Evaluate for malaria.
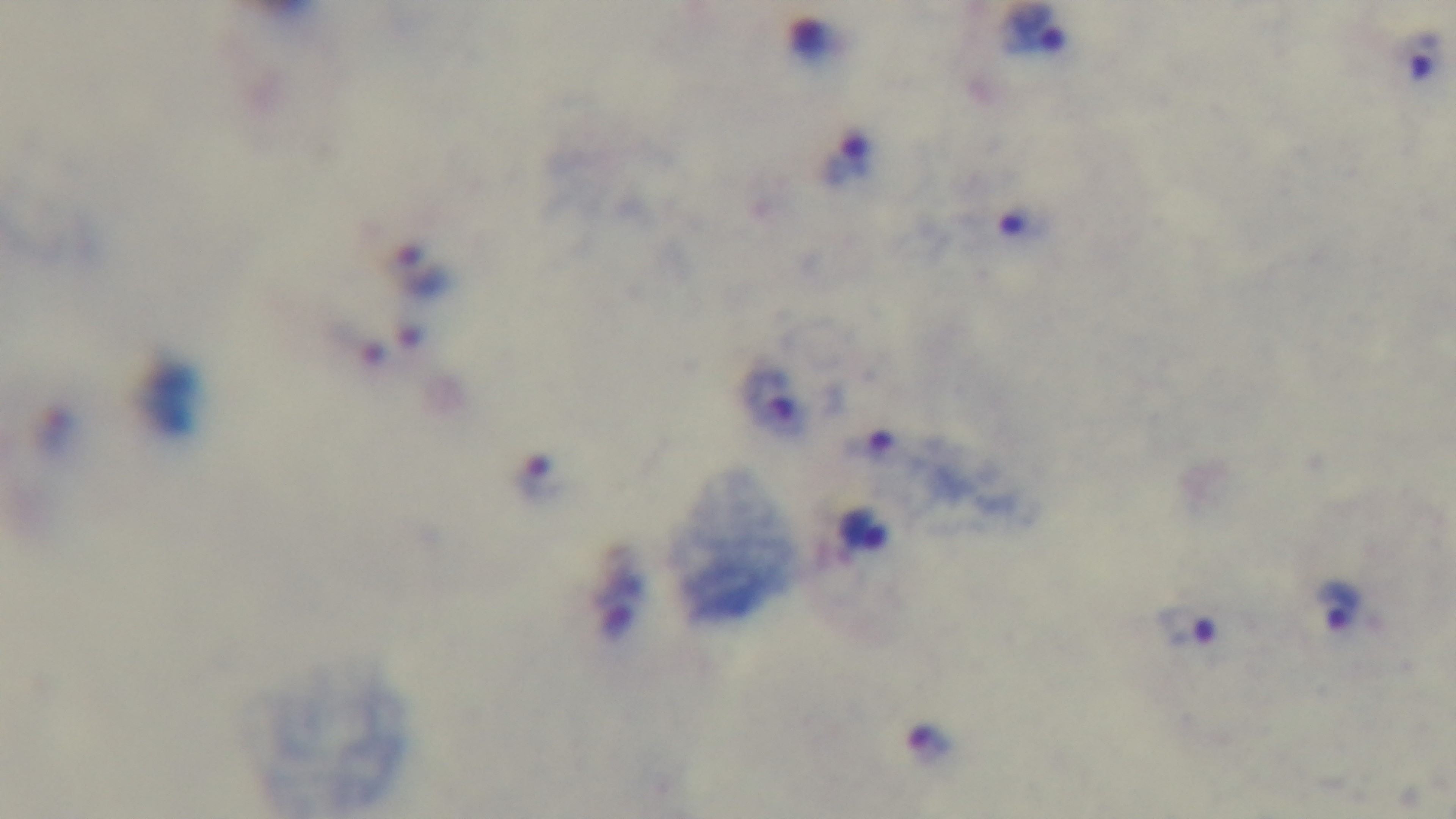

Infected.

capture = mounted 4K digital camera
stain = Giemsa
objective = 100x oil immersion
modality = light microscopy
preparation = thick
field of view = single